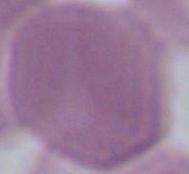

Summary:
  - Modality: micrograph
  - Identification: red blood cell
  - Magnification: 1000x